Report the malaria status of this cell.
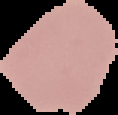
Uninfected.

Summary:
  - Image type: segmented cell region with the area outside set to black
  - Image size: 118×115 pixels
  - Preparation: thin blood smear